Give the location of every parasitized red blood cell.
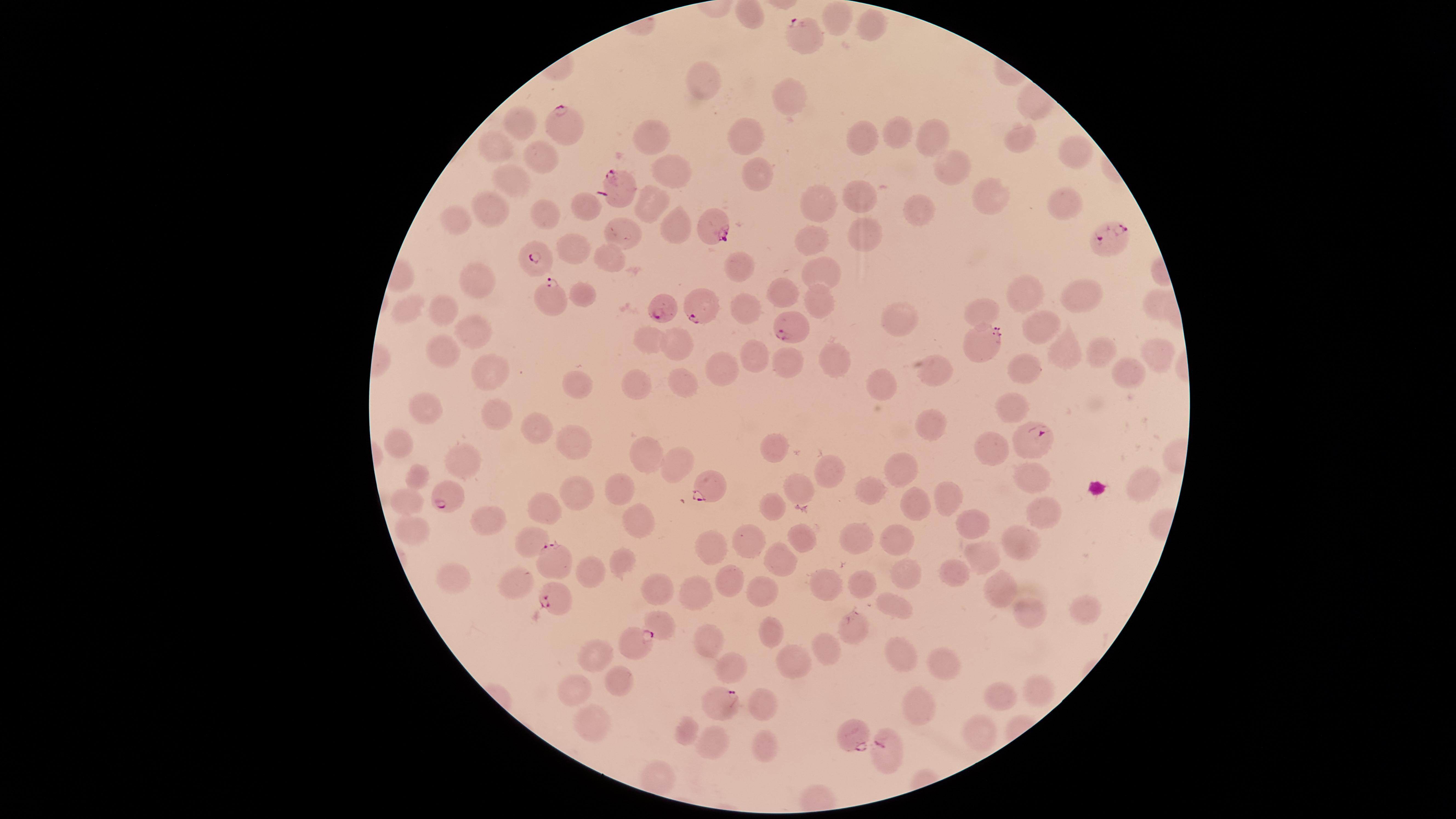
Approximate marker points as [x, y] in pixels.
Parasitized red blood cells: [807, 27], [563, 127], [621, 187], [710, 222], [1109, 236], [535, 261], [546, 298], [704, 305], [664, 307], [788, 328], [983, 344], [1033, 441], [708, 485], [453, 496], [551, 559], [557, 596], [625, 643], [719, 699], [849, 733], [884, 750].

Approximate marker points as [x, y] in pixels.
Summary:
  - Uninfected red blood cells: [840, 16], [868, 28], [708, 88], [793, 95], [519, 126], [753, 134], [902, 134], [862, 138], [656, 139], [935, 139], [1017, 141], [495, 147], [1074, 149], [541, 161], [949, 168], [673, 170], [511, 178], [758, 180], [989, 196], [810, 197], [619, 199], [860, 200], [654, 202], [1062, 204], [583, 206], [918, 211], [491, 212], [544, 219], [456, 222], [674, 224], [627, 235], [865, 235], [815, 239], [573, 248], [615, 257], [740, 267], [824, 269], [481, 284], [584, 296], [786, 296], [1028, 297], [1086, 297], [823, 300], [413, 307], [750, 308], [448, 309], [985, 312], [476, 322], [903, 323], [1039, 328], [653, 343], [675, 349], [1060, 350], [1158, 350], [446, 353], [1092, 353], [835, 357], [788, 361], [728, 362], [488, 363], [1020, 368], [936, 370], [1125, 372], [680, 382], [580, 383], [882, 384], [637, 389], [1016, 398], [430, 413], [497, 417], [932, 419], [539, 428], [404, 442], [576, 446], [780, 447], [999, 447], [650, 462], [462, 466], [678, 467], [905, 467], [419, 474], [828, 474], [1032, 482], [873, 488], [626, 489], [800, 489], [1144, 489], [942, 496], [578, 498], [411, 500], [918, 506], [544, 512], [775, 512], [476, 518], [1041, 522], [641, 524], [968, 524], [417, 526], [860, 535], [803, 536], [898, 537], [1015, 538], [531, 539], [753, 540], [716, 554], [788, 556], [981, 559], [621, 565], [586, 571], [948, 575], [905, 577], [734, 578], [459, 579], [657, 586], [829, 586], [863, 586], [763, 588], [517, 589], [999, 591], [691, 592], [888, 607], [1026, 611], [1086, 612], [657, 626], [769, 630], [854, 633], [829, 641], [707, 643], [596, 647], [897, 660], [795, 661], [942, 662], [729, 669], [622, 679], [581, 689], [1036, 691], [999, 694], [760, 704], [924, 705], [596, 722], [688, 729], [980, 733], [721, 742], [763, 751]
  - Preparation: thin smear of blood
  - Capture: smartphone photograph through the microscope eyepiece
  - Species: Plasmodium falciparum
  - Image size: 1456×819 pixels
  - Field of view: single
  - Stain: Giemsa
  - Visible region: circular